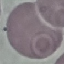 Malaria status: uninfected. Thin blood film. Automatically extracted cell patch, resized to 64 × 64 pixels. Photographed with a smartphone camera at the microscope eyepiece. Giemsa stain.